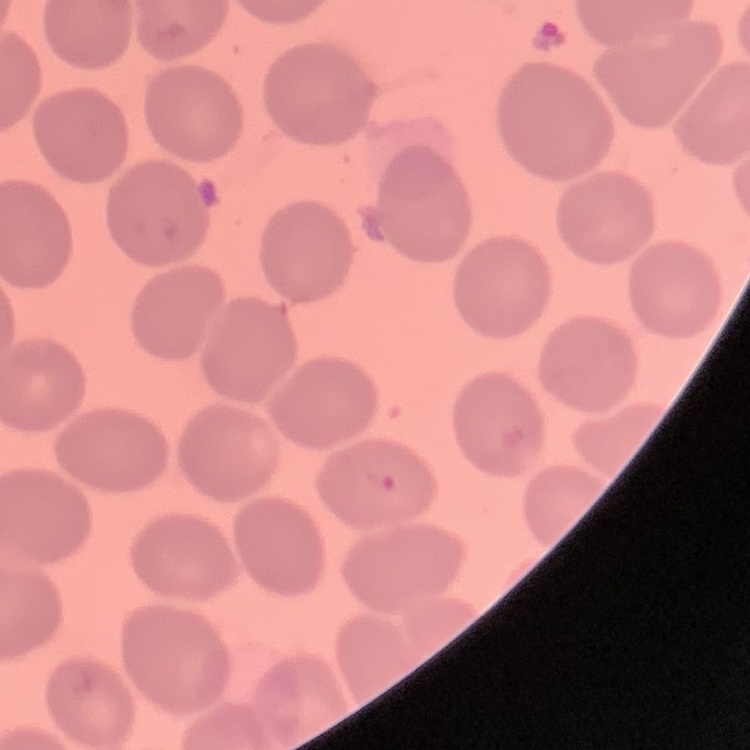

The red blood cells show no rouleaux formation. Stained with either Field's or Giemsa. Thin blood film. One tile cut from a larger photomicrograph.